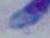
Toxoplasma gondii is seen. Micrograph. Captured at 1000x magnification.